Locate platelets.
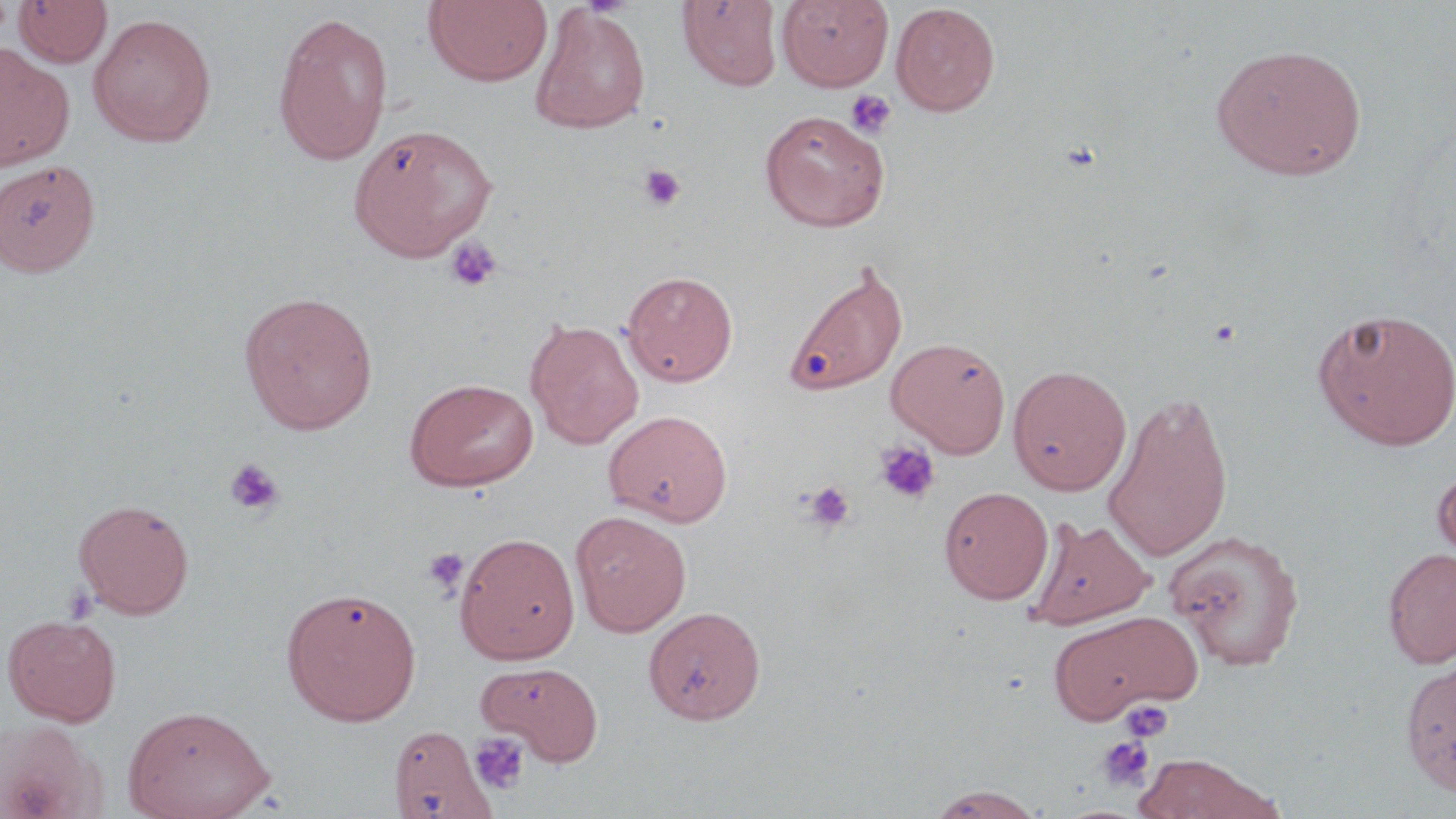
Approximate bounding boxes as (x1, y1, x2, y2) in pixels.
Platelets: (846, 89, 896, 139), (638, 164, 685, 211), (444, 237, 501, 292), (1208, 318, 1243, 348), (874, 441, 941, 505), (224, 458, 285, 517), (803, 481, 855, 533), (422, 547, 470, 597), (1119, 699, 1174, 742), (469, 732, 530, 795), (1097, 737, 1155, 793).

Uninfected red blood cell locations: (10, 0, 110, 67), (423, 0, 553, 87), (777, 0, 893, 91), (677, 1, 783, 91), (891, 2, 1001, 116), (529, 4, 651, 134), (272, 12, 394, 165), (88, 13, 217, 148), (1211, 43, 1366, 180), (0, 45, 75, 170), (759, 109, 890, 232), (349, 122, 497, 260), (0, 160, 100, 277), (784, 261, 908, 398), (622, 270, 738, 387), (238, 290, 378, 434), (1313, 307, 1456, 450), (526, 318, 644, 450), (886, 337, 1010, 457), (1007, 364, 1132, 496), (404, 378, 538, 491), (1103, 391, 1233, 562), (603, 409, 733, 527), (1431, 461, 1456, 571), (939, 486, 1053, 604), (73, 498, 194, 618), (570, 510, 692, 637), (1028, 515, 1155, 629), (1165, 528, 1305, 671), (454, 531, 580, 663), (1382, 547, 1456, 668), (281, 586, 421, 725), (644, 605, 766, 725), (1046, 609, 1203, 724), (2, 613, 122, 726), (1400, 659, 1456, 796), (476, 660, 604, 764), (123, 703, 275, 818), (0, 720, 101, 818), (390, 733, 498, 819), (1134, 753, 1271, 818), (925, 785, 1045, 819). Slide-level diagnosis: no evidence of blood parasites. May-Grünwald-Giemsa-stained preparation. One field of a larger specimen. Light microscopy. Image is 1456×819 pixels. Thin blood film. 1000x magnification.